Point out each Plasmodium parasite.
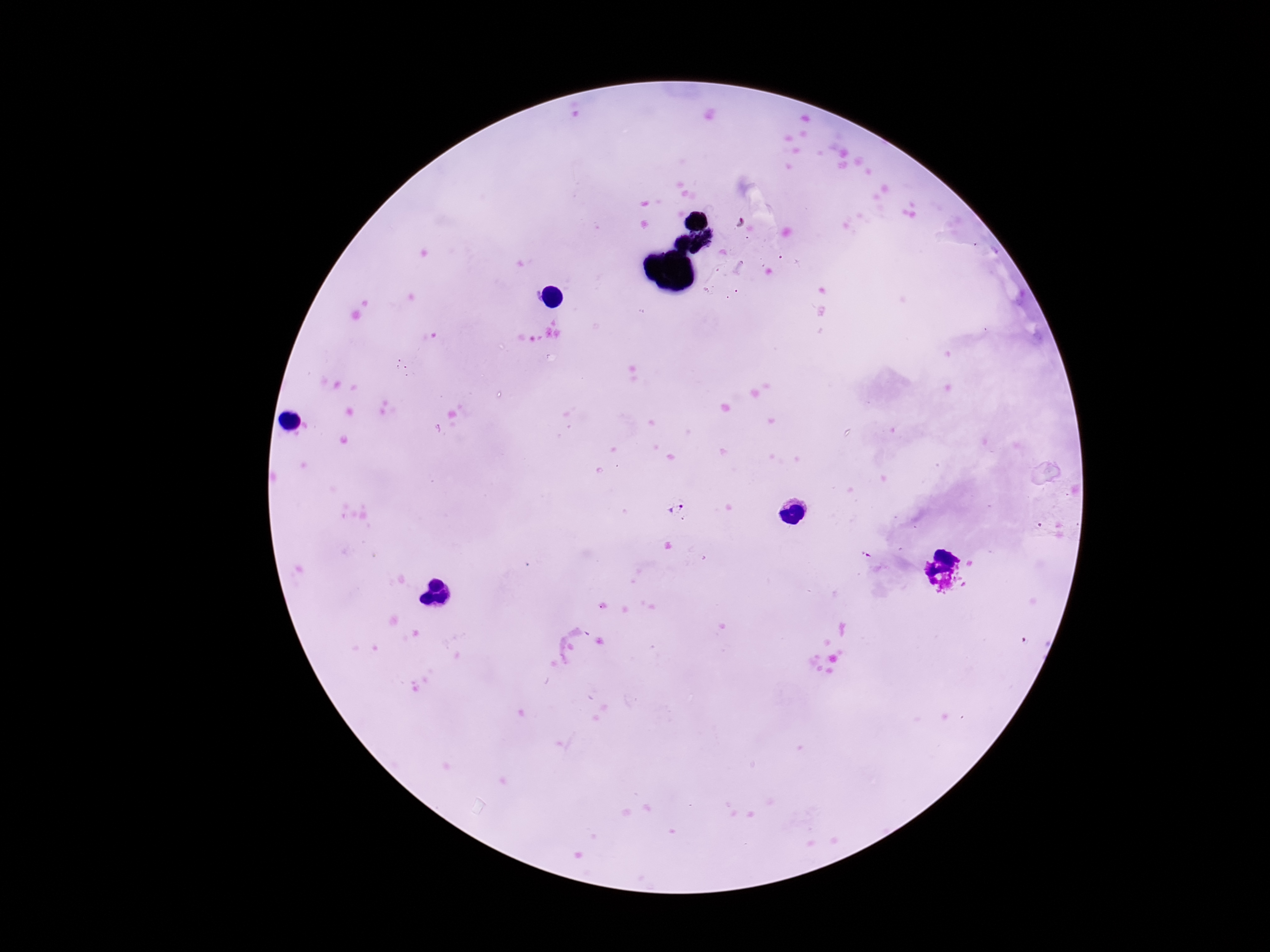

Approximate centers as {x, y} in pixels.
Plasmodium parasites: {675, 507}.

Image is 1270×952 pixels. Giemsa-stained preparation. Thick peripheral-blood smear. Patient malaria status: infected. Photographed through the microscope eyepiece with a smartphone camera. 100x magnification. One field from this slide.